Assess this cell for malaria.
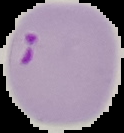
Parasitized.

image_size: 124×133 pixels
preparation: thin blood smear
image_type: segmented cell region on a black background